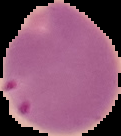
Result: Plasmodium parasites identified. Image is 121×136 pixels. Segmented cell region on a black background. From a thin blood smear.